Comment on the morphology of the red blood cells.
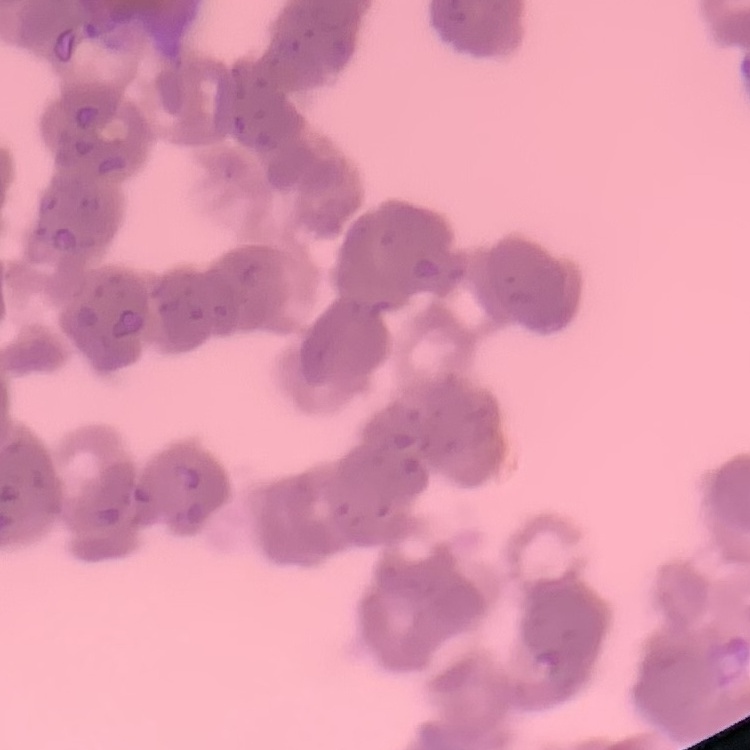
Rouleaux formation.

preparation = thin blood film
image type = square crop of a larger photomicrograph
stain = Field's or Giemsa